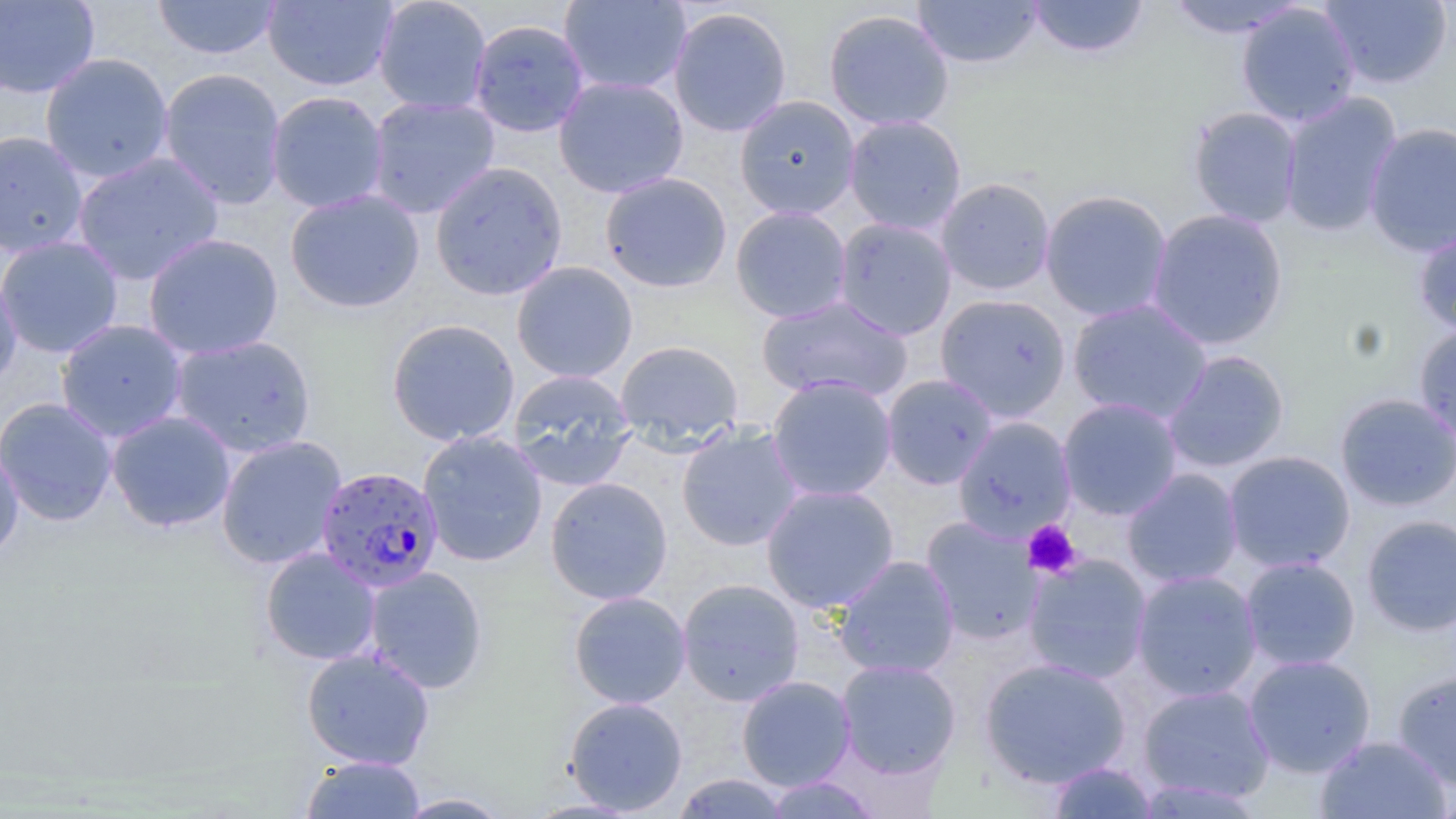
slide-level diagnosis = Plasmodium falciparum
image size = 1456×819 pixels
uninfected red blood cell locations = approximate bounding boxes as named x1/y1/x2/y2 corners in pixels: (x1=151, y1=0, x2=282, y2=61), (x1=262, y1=0, x2=397, y2=91), (x1=373, y1=0, x2=493, y2=115), (x1=558, y1=0, x2=692, y2=96), (x1=911, y1=0, x2=1045, y2=69), (x1=1026, y1=0, x2=1150, y2=59), (x1=1319, y1=0, x2=1453, y2=90), (x1=0, y1=1, x2=100, y2=99), (x1=1162, y1=1, x2=1310, y2=39), (x1=1236, y1=3, x2=1361, y2=127), (x1=667, y1=6, x2=793, y2=137), (x1=823, y1=8, x2=955, y2=132), (x1=468, y1=19, x2=590, y2=138), (x1=40, y1=52, x2=174, y2=183), (x1=157, y1=67, x2=287, y2=210), (x1=553, y1=75, x2=689, y2=199), (x1=266, y1=91, x2=389, y2=213), (x1=1279, y1=92, x2=1403, y2=237), (x1=366, y1=95, x2=501, y2=218), (x1=734, y1=95, x2=860, y2=219), (x1=1187, y1=106, x2=1303, y2=228), (x1=843, y1=115, x2=967, y2=235), (x1=1364, y1=121, x2=1456, y2=256), (x1=0, y1=130, x2=89, y2=259), (x1=72, y1=152, x2=224, y2=284), (x1=430, y1=160, x2=568, y2=301), (x1=600, y1=172, x2=733, y2=293), (x1=936, y1=177, x2=1056, y2=295), (x1=1040, y1=189, x2=1173, y2=322), (x1=285, y1=190, x2=424, y2=313), (x1=730, y1=205, x2=852, y2=323), (x1=1146, y1=208, x2=1289, y2=350), (x1=833, y1=217, x2=957, y2=340), (x1=1413, y1=221, x2=1456, y2=340), (x1=143, y1=233, x2=284, y2=359), (x1=0, y1=236, x2=124, y2=358), (x1=511, y1=261, x2=638, y2=383), (x1=0, y1=265, x2=22, y2=390), (x1=934, y1=293, x2=1071, y2=421), (x1=756, y1=295, x2=913, y2=403), (x1=1067, y1=299, x2=1213, y2=424), (x1=386, y1=318, x2=521, y2=446), (x1=55, y1=319, x2=189, y2=443), (x1=1413, y1=324, x2=1456, y2=448), (x1=168, y1=334, x2=317, y2=458), (x1=615, y1=339, x2=744, y2=447), (x1=1162, y1=350, x2=1290, y2=473), (x1=507, y1=369, x2=637, y2=490), (x1=882, y1=374, x2=998, y2=489), (x1=767, y1=376, x2=898, y2=502), (x1=1334, y1=392, x2=1456, y2=512), (x1=0, y1=397, x2=119, y2=527), (x1=1058, y1=397, x2=1183, y2=520), (x1=106, y1=411, x2=236, y2=533), (x1=953, y1=416, x2=1077, y2=542), (x1=676, y1=425, x2=804, y2=552), (x1=418, y1=430, x2=548, y2=567), (x1=216, y1=435, x2=347, y2=570), (x1=0, y1=441, x2=24, y2=565), (x1=1222, y1=450, x2=1356, y2=573), (x1=1121, y1=468, x2=1244, y2=588), (x1=545, y1=477, x2=673, y2=604), (x1=760, y1=483, x2=899, y2=613), (x1=1361, y1=515, x2=1456, y2=637), (x1=921, y1=516, x2=1043, y2=644), (x1=260, y1=547, x2=381, y2=666), (x1=1023, y1=554, x2=1153, y2=684), (x1=832, y1=555, x2=960, y2=679), (x1=1240, y1=556, x2=1361, y2=671), (x1=364, y1=566, x2=489, y2=693), (x1=1131, y1=570, x2=1262, y2=701), (x1=676, y1=578, x2=805, y2=707), (x1=568, y1=591, x2=691, y2=709), (x1=301, y1=647, x2=435, y2=770), (x1=1243, y1=654, x2=1376, y2=778), (x1=979, y1=657, x2=1131, y2=788), (x1=836, y1=659, x2=961, y2=779), (x1=1392, y1=669, x2=1456, y2=790), (x1=736, y1=675, x2=856, y2=791), (x1=1137, y1=684, x2=1275, y2=804), (x1=563, y1=696, x2=688, y2=815), (x1=1314, y1=735, x2=1453, y2=819), (x1=300, y1=755, x2=426, y2=818), (x1=1046, y1=761, x2=1158, y2=818), (x1=671, y1=773, x2=791, y2=818), (x1=762, y1=775, x2=881, y2=818), (x1=1434, y1=782, x2=1456, y2=819), (x1=394, y1=792, x2=513, y2=818)
magnification = 1000x
field of view = one of a larger specimen
preparation = thin blood film
modality = optical microscopy
stain = May-Grünwald-Giemsa
Plasmodium falciparum-infected red blood cell locations = approximate bounding boxes as named x1/y1/x2/y2 corners in pixels: (x1=315, y1=465, x2=444, y2=592)
platelet locations = approximate bounding boxes as named x1/y1/x2/y2 corners in pixels: (x1=1023, y1=520, x2=1082, y2=579)